Assess this cell for malaria.
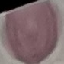
It is uninfected.

Giemsa stain. Automatically extracted cell patch, resized to 64 × 64 pixels. Thin blood film. Acquired by smartphone through the microscope eyepiece.